Locate platelets.
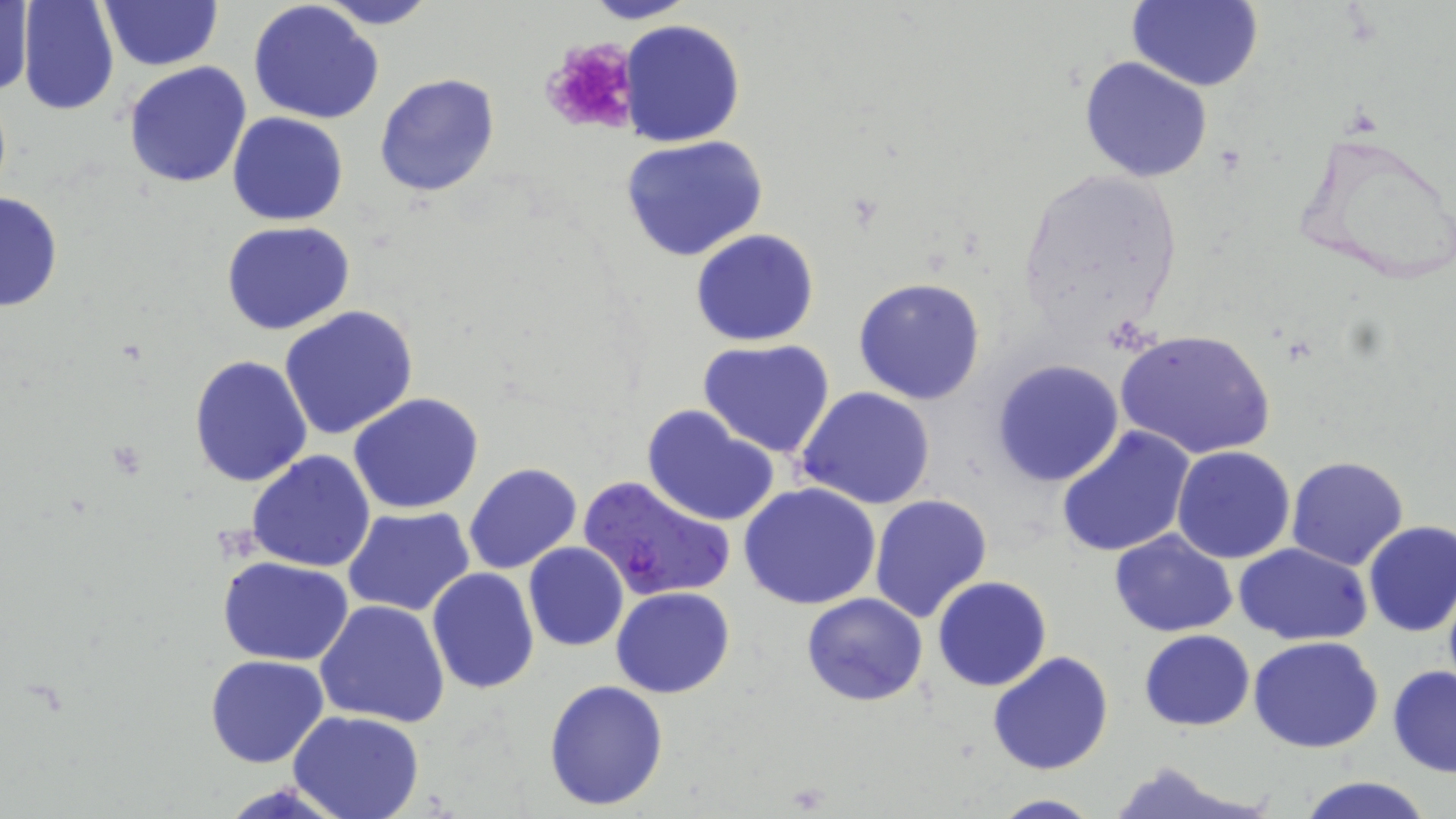

Approximate bounding boxes as (x1, y1, x2, y2) in pixels.
Platelets: (540, 37, 638, 137).

slide-level diagnosis = Plasmodium falciparum
magnification = 1000x
field of view = single
image size = 1456×819 pixels
uninfected red blood cell locations = approximate bounding boxes as (x1, y1, x2, y2) in pixels: (17, 0, 121, 117), (99, 0, 219, 70), (313, 0, 439, 29), (581, 0, 699, 24), (1126, 0, 1262, 91), (1, 1, 32, 102), (248, 1, 384, 124), (621, 19, 746, 148), (1079, 56, 1212, 182), (122, 60, 253, 189), (373, 72, 501, 198), (227, 112, 348, 225), (1289, 125, 1456, 288), (622, 134, 770, 263), (1011, 167, 1186, 347), (0, 191, 63, 314), (221, 222, 356, 336), (690, 228, 820, 347), (853, 277, 987, 405), (278, 305, 419, 441), (1114, 329, 1275, 463), (697, 339, 837, 458), (187, 355, 313, 487), (989, 359, 1125, 487), (794, 387, 937, 511), (347, 391, 484, 513), (642, 404, 781, 527), (1056, 426, 1195, 558), (1171, 446, 1297, 564), (246, 449, 376, 572), (1285, 456, 1411, 572), (462, 462, 582, 574), (739, 483, 882, 610), (869, 493, 993, 622), (342, 506, 476, 617), (1362, 521, 1456, 637), (1109, 528, 1238, 638), (522, 543, 629, 651), (1233, 543, 1373, 645), (217, 556, 354, 666), (425, 568, 540, 695), (932, 576, 1053, 692), (1441, 582, 1456, 701), (610, 586, 736, 698), (801, 593, 929, 707), (314, 599, 449, 728), (1139, 630, 1255, 730), (1248, 637, 1386, 754), (987, 650, 1113, 776), (205, 655, 328, 768), (1387, 666, 1456, 777), (542, 678, 670, 811), (288, 710, 425, 819), (1103, 761, 1266, 819), (1294, 775, 1439, 819), (986, 794, 1105, 818)
stain = May-Grünwald-Giemsa
preparation = thin blood smear
Plasmodium falciparum-infected red blood cell locations = approximate bounding boxes as (x1, y1, x2, y2) in pixels: (577, 475, 736, 602)
modality = optical microscopy